State which parasite is depicted.
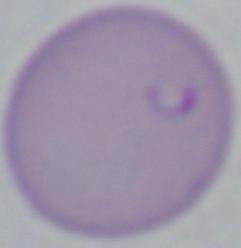

This is Babesia.

Summary:
  - Modality: photomicrograph
  - Magnification: 1000x